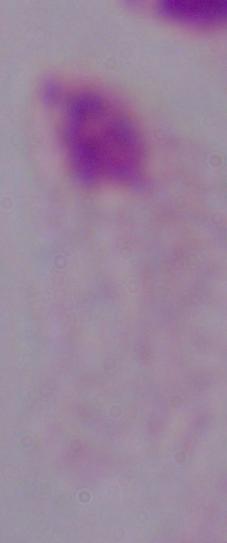 A trichomonad is seen. Captured at 1000x magnification. Photomicrograph.